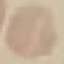 Result: negative for malaria parasites. Automatically extracted cell patch, resized to 64 × 64 pixels. Giemsa stain. Acquired by smartphone through the microscope eyepiece. Thin smear of blood.